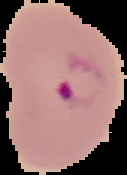
{
  "image_type": "cell region segmented out of the field of view; surrounding area masked to black",
  "preparation": "thin blood smear",
  "result": "Plasmodium parasites detected",
  "image_size": "127×175 pixels"
}